Assess this cell for malaria.
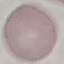
Uninfected.

Giemsa stain. Cell patch, automatically extracted from a larger field of view and resized to 64 × 64 pixels. Thin blood smear. Acquired by smartphone through the microscope eyepiece.